Locate every Plasmodium vivax-infected red blood cell.
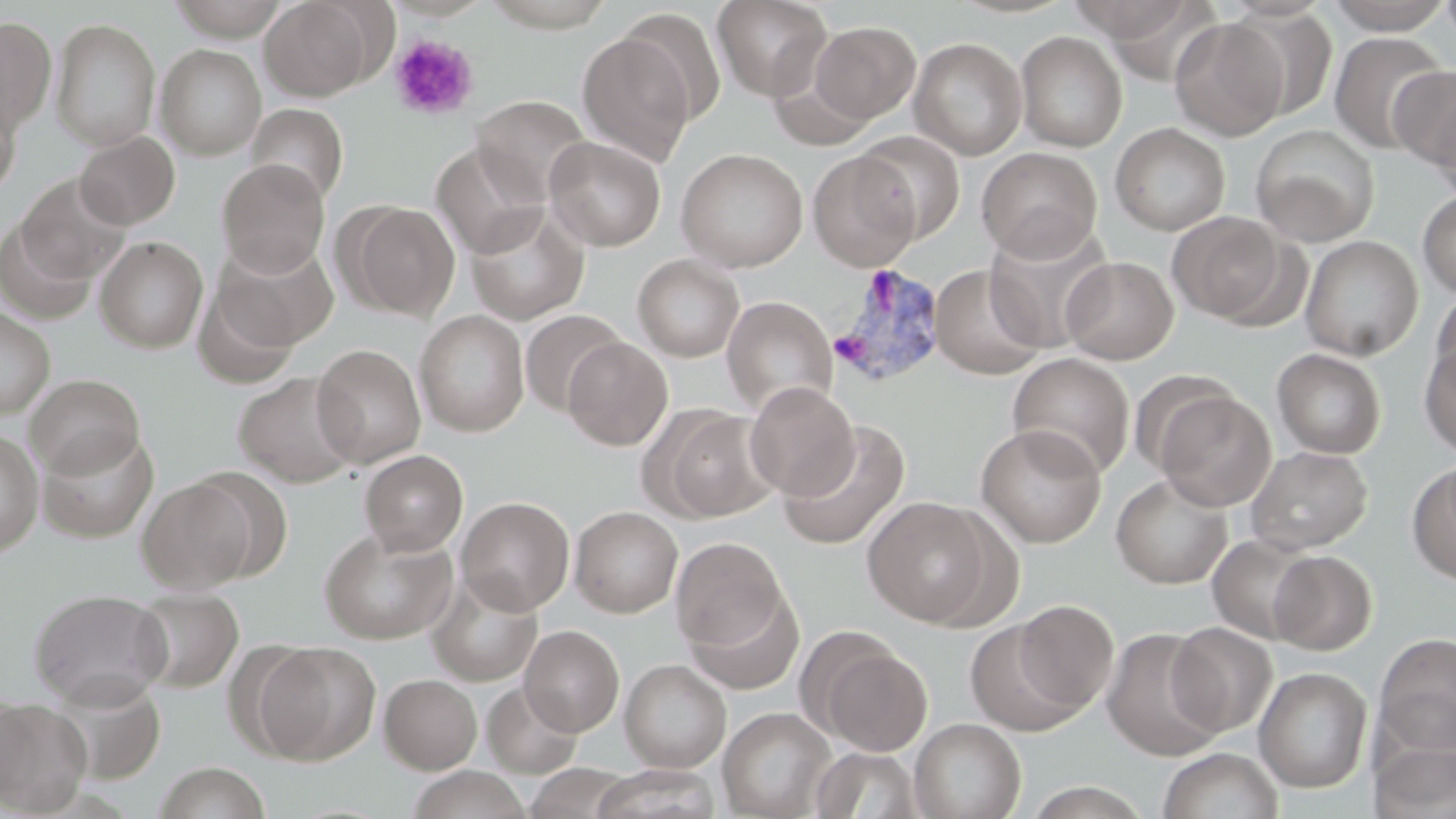

Approximate bounding boxes as (x1,y1)-(x2,y2) corner pairs in pixels.
Plasmodium vivax-infected red blood cells: (827,263)-(949,390).

Summary:
  - Uninfected red blood cell locations: (167,0)-(291,42), (259,0)-(377,101), (384,0)-(491,21), (480,0)-(619,32), (711,0)-(831,100), (1075,0)-(1212,54), (1322,0)-(1455,34), (1438,0)-(1456,48), (615,8)-(728,127), (1225,8)-(1339,123), (0,15)-(57,134), (1169,16)-(1290,141), (51,18)-(161,151), (808,21)-(921,125), (1014,30)-(1127,152), (575,31)-(697,167), (1327,31)-(1451,155), (908,36)-(1028,160), (155,43)-(267,160), (1389,67)-(1456,175), (0,89)-(21,199), (1430,94)-(1456,200), (471,95)-(592,203), (245,103)-(349,205), (1110,122)-(1230,236), (1249,124)-(1380,247), (74,131)-(180,230), (854,131)-(966,244), (544,136)-(666,251), (430,142)-(550,258), (976,146)-(1103,261), (675,148)-(808,272), (807,149)-(922,270), (217,159)-(330,276), (16,174)-(132,287), (1416,189)-(1456,299), (342,202)-(460,320), (465,207)-(590,326), (1167,211)-(1292,326), (0,216)-(99,325), (984,222)-(1115,353), (1300,235)-(1423,361), (94,236)-(208,353), (212,238)-(339,353), (632,254)-(745,362), (1061,256)-(1179,364), (929,263)-(1046,380), (192,270)-(305,389), (1429,291)-(1456,391), (721,295)-(837,417), (0,306)-(55,419), (520,309)-(628,417), (414,310)-(529,437), (562,336)-(673,451), (311,344)-(426,469), (1419,344)-(1456,457), (1272,348)-(1386,459), (1007,352)-(1135,479), (232,372)-(362,488), (25,373)-(146,479), (744,381)-(859,501), (1152,388)-(1277,511), (651,406)-(779,522), (776,420)-(912,551), (975,423)-(1107,547), (0,428)-(44,557), (37,429)-(159,544), (1245,445)-(1373,554), (360,449)-(468,556), (1408,462)-(1456,583), (1110,472)-(1233,589), (136,476)-(259,594), (862,496)-(1001,627), (456,497)-(575,615), (570,506)-(683,618), (318,527)-(458,644), (1207,533)-(1319,645), (671,537)-(790,656), (1268,550)-(1377,655), (426,572)-(544,687), (683,584)-(805,695), (130,588)-(244,693), (28,589)-(172,710), (1011,600)-(1119,714), (964,618)-(1087,736), (1166,622)-(1277,737), (519,625)-(624,736), (1100,627)-(1226,762), (805,632)-(934,757), (1373,632)-(1456,757), (254,641)-(381,764), (619,658)-(732,774), (1253,667)-(1372,794), (379,673)-(482,774), (47,677)-(167,784), (481,681)-(583,779), (0,692)-(29,804), (0,699)-(91,816), (718,707)-(836,819), (909,717)-(1026,819), (1371,738)-(1456,819), (810,746)-(926,818), (1157,747)-(1284,819), (152,761)-(272,819), (403,766)-(532,819), (587,766)-(722,819), (1021,781)-(1155,819)
  - Platelet locations: (389,34)-(479,121)
  - Slide-level diagnosis: Plasmodium vivax
  - Magnification: 1000x
  - Preparation: thin blood smear
  - Image size: 1456×819 pixels
  - Modality: light microscopy
  - Field of view: one of a larger specimen
  - Stain: May-Grünwald-Giemsa